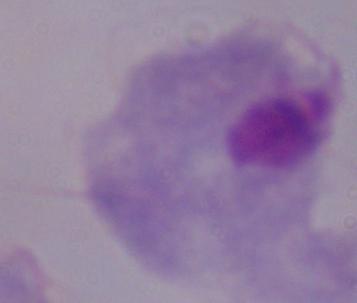
modality: micrograph
identification: trichomonad
magnification: 1000x